Assess the morphology of the erythrocytes.
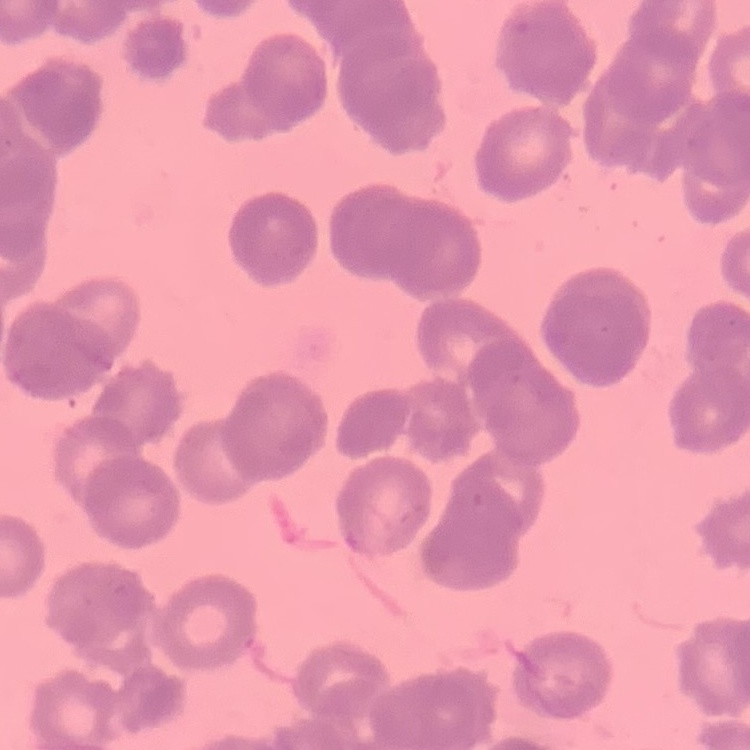
Rouleaux formation.

Stained with either Field's or Giemsa. Thin peripheral smear. Square crop of a larger photomicrograph.